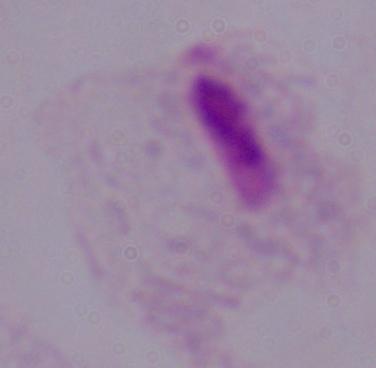

identification = trichomonad
modality = photomicrograph
magnification = 1000x